Comment on the morphology of the erythrocytes.
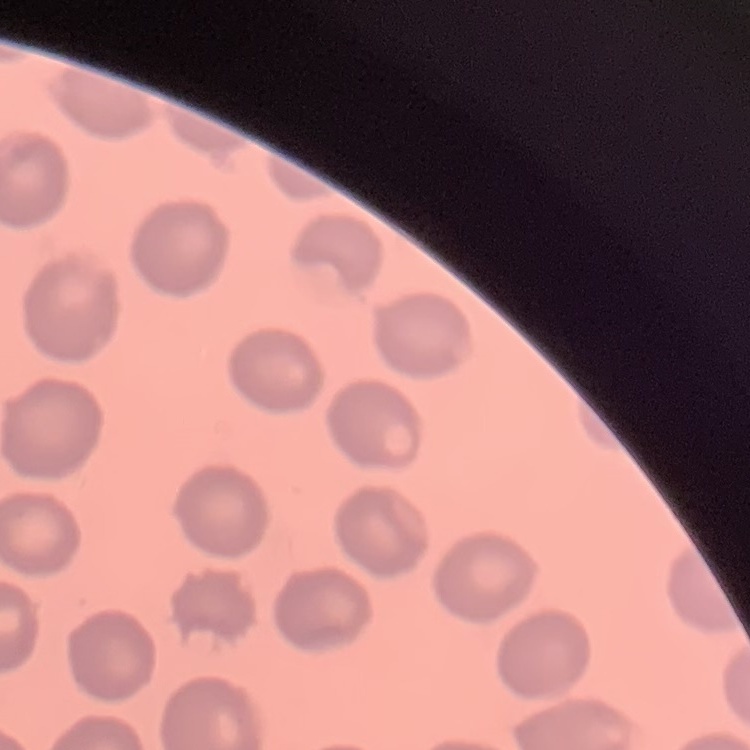

No rouleaux formation.

{
  "image_type": "one tile cut from a larger photomicrograph",
  "preparation": "thin blood smear",
  "stain": "Field's or Giemsa"
}